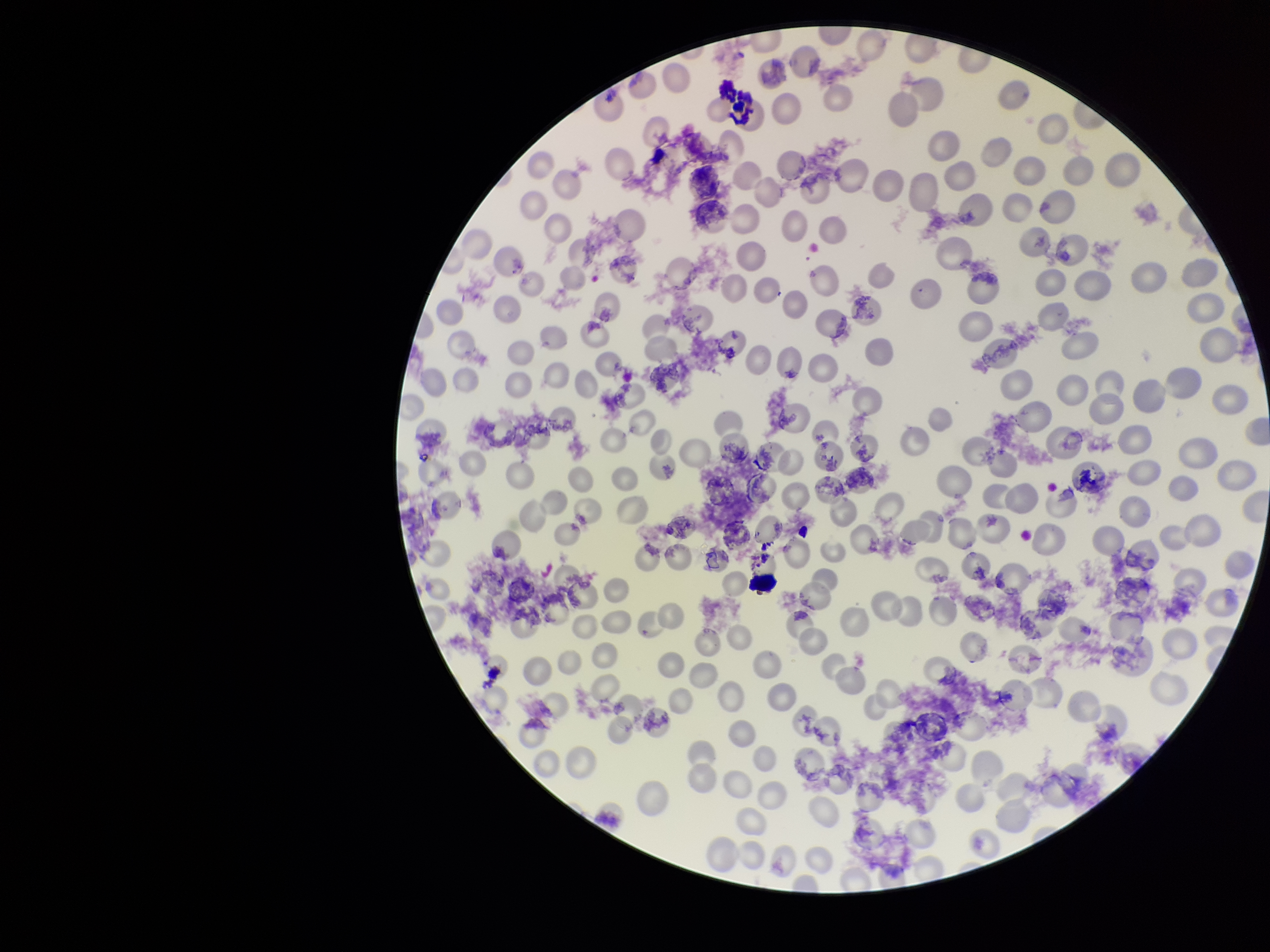
capture: smartphone photograph through the microscope eyepiece
patient_malaria_status: positive
stain: Giemsa
red_blood_cell_count: 210
parasitized_red_blood_cells: none seen
parasitized_red_blood_cell_count: 0
species_reported_for_this_patient: Plasmodium vivax
image_size: 1270×952 pixels
preparation: thin
field_of_view: single